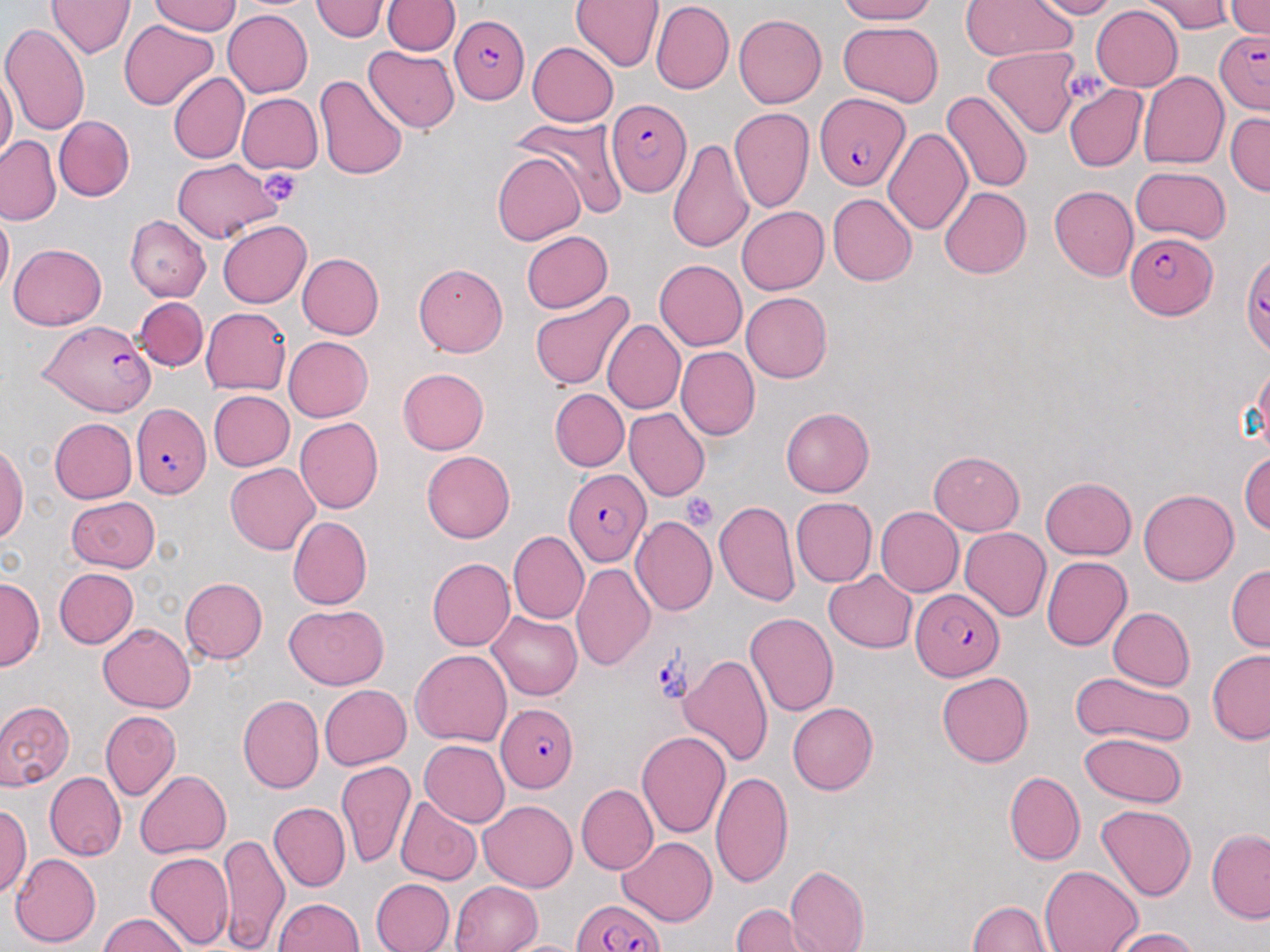
Approximate bounding boxes as [x1, y1, x2, y2] in pixels. Platelet locations: [259, 167, 303, 206], [681, 492, 721, 530]. Plasmodium falciparum-infected red blood cell locations: [451, 14, 527, 105], [1213, 29, 1270, 115], [814, 93, 908, 190], [605, 100, 692, 197], [1125, 233, 1217, 318], [1240, 251, 1270, 357], [41, 319, 157, 416], [131, 403, 211, 499], [564, 468, 651, 565], [910, 588, 1006, 681], [496, 702, 579, 791], [572, 899, 663, 952]. Uninfected red blood cell locations: [47, 0, 135, 58], [310, 0, 390, 41], [383, 0, 459, 55], [569, 0, 664, 71], [835, 0, 935, 25], [1026, 0, 1118, 19], [1140, 0, 1231, 35], [1225, 0, 1270, 40], [150, 1, 241, 36], [652, 1, 734, 94], [961, 1, 1077, 61], [1091, 5, 1184, 92], [223, 9, 313, 98], [734, 13, 827, 107], [119, 19, 218, 111], [839, 20, 943, 107], [0, 23, 90, 136], [528, 43, 619, 126], [363, 46, 459, 133], [979, 46, 1082, 135], [0, 68, 17, 165], [1138, 71, 1229, 169], [169, 72, 249, 163], [314, 74, 408, 181], [1063, 85, 1148, 171], [941, 90, 1033, 194], [237, 92, 323, 174], [729, 108, 814, 214], [1227, 113, 1269, 195], [54, 115, 134, 202], [514, 115, 629, 219], [884, 127, 973, 235], [0, 135, 60, 225], [666, 135, 754, 255], [492, 152, 586, 246], [171, 158, 281, 243], [1131, 166, 1230, 244], [1049, 185, 1138, 281], [940, 187, 1031, 278], [828, 193, 917, 286], [737, 206, 828, 295], [0, 209, 13, 296], [125, 216, 211, 301], [218, 220, 311, 308], [521, 231, 612, 312], [8, 243, 107, 331], [297, 253, 384, 339], [655, 260, 747, 351], [414, 263, 508, 357], [528, 289, 634, 391], [741, 292, 832, 383], [134, 297, 208, 371], [201, 307, 291, 395], [602, 319, 684, 415], [283, 336, 373, 421], [675, 346, 760, 441], [1254, 360, 1270, 453], [397, 367, 489, 454], [550, 388, 629, 471], [208, 391, 295, 472], [623, 407, 710, 501], [781, 407, 874, 496], [294, 417, 383, 514], [50, 418, 136, 503], [0, 444, 28, 545], [928, 450, 1025, 536], [421, 451, 515, 542], [1240, 451, 1269, 535], [225, 462, 319, 554], [1041, 476, 1136, 559], [1138, 489, 1238, 585], [67, 496, 160, 573], [791, 497, 877, 588], [714, 500, 800, 607], [876, 506, 964, 597], [287, 516, 371, 609], [631, 516, 717, 616], [960, 527, 1051, 623], [508, 530, 589, 624], [1042, 556, 1131, 651], [427, 558, 515, 651], [571, 563, 654, 670], [1226, 564, 1269, 652], [54, 568, 139, 649], [823, 570, 917, 652], [0, 577, 43, 671], [180, 577, 267, 663], [284, 604, 390, 689], [1107, 607, 1194, 690], [487, 612, 582, 701], [744, 612, 839, 717], [99, 623, 195, 712], [411, 649, 511, 746], [1206, 649, 1270, 744], [680, 653, 775, 767], [1070, 671, 1196, 749], [937, 672, 1033, 767], [319, 685, 412, 770], [239, 694, 323, 794], [0, 700, 74, 792], [787, 702, 877, 794], [100, 711, 180, 801], [636, 730, 732, 839], [1079, 732, 1187, 808], [419, 740, 510, 826], [337, 761, 415, 869], [136, 770, 231, 859], [710, 771, 793, 889], [1003, 771, 1084, 866], [45, 772, 126, 860], [576, 783, 657, 875], [395, 797, 482, 885], [1, 801, 32, 897], [478, 801, 577, 891], [268, 802, 350, 892], [1097, 805, 1196, 901], [1206, 829, 1270, 923], [218, 833, 289, 952], [618, 837, 717, 927], [145, 852, 234, 950], [10, 853, 103, 948], [786, 865, 869, 952], [1040, 865, 1142, 951], [371, 878, 455, 952], [451, 880, 542, 951], [273, 898, 364, 951], [969, 900, 1052, 952], [732, 903, 823, 952], [99, 912, 190, 951], [1109, 928, 1200, 951], [500, 939, 593, 952]. Slide-level diagnosis: Plasmodium falciparum. Captured at 1000x magnification. Image is 1270×952 pixels. Thin blood smear. One field of a larger specimen. May-Grünwald-Giemsa-stained preparation. Light microscopy.